Comment on the morphology of the red blood cells.
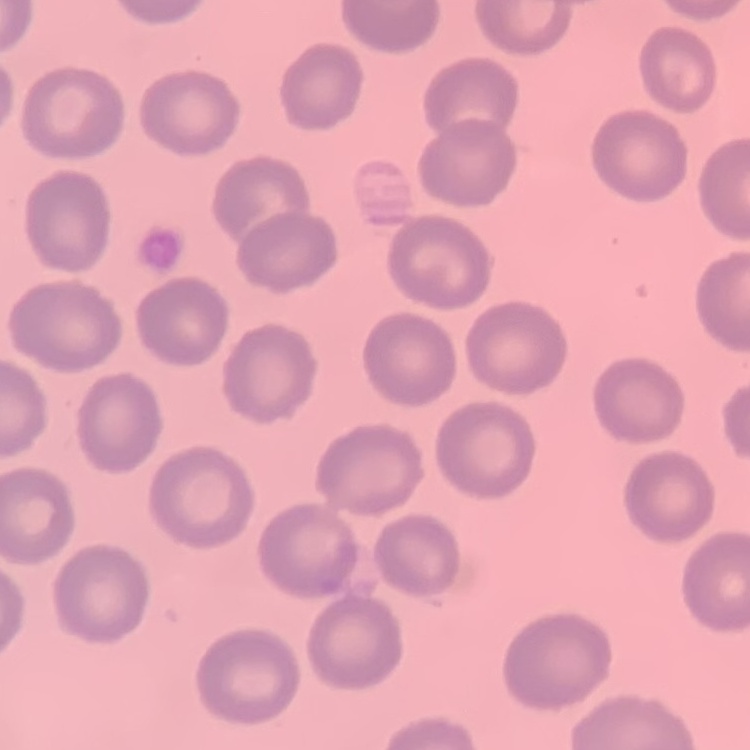
They show no rouleaux formation.

Field's or Giemsa stain. Square crop of a larger photomicrograph. Thin blood film.